Classify this cell by malaria status.
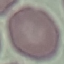

Uninfected.

Giemsa stain. Automatically extracted cell patch, resized to 64 × 64 pixels. Thin smear of blood. Photographed with a smartphone camera at the microscope eyepiece.